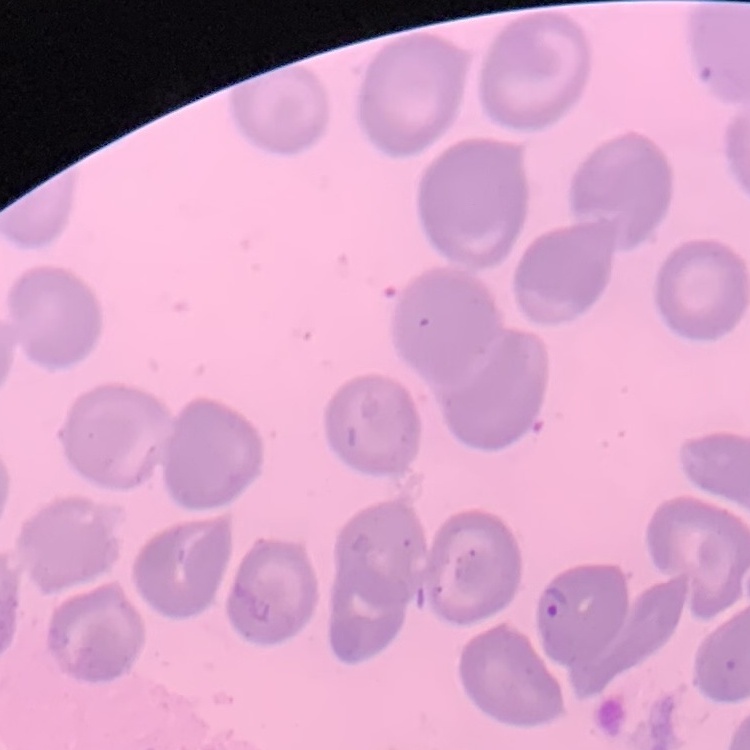
Summary:
  - Erythrocyte morphology: no rouleaux formation
  - Preparation: thin peripheral smear
  - Stain: Field's or Giemsa
  - Image type: one tile cut from a larger photomicrograph